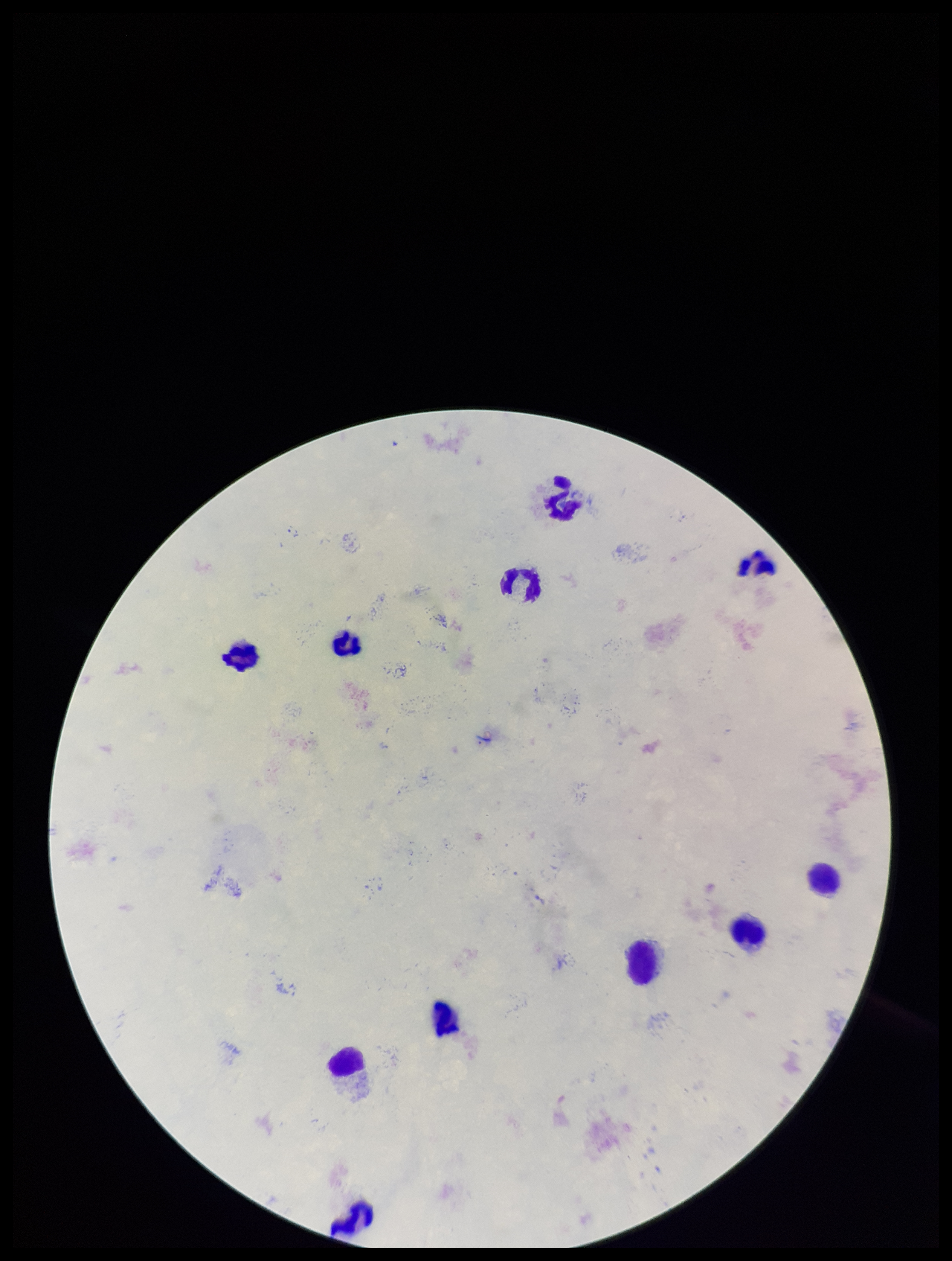

Leukocyte count: 11. Plasmodium parasites: none identified. Preparation: thick smear. Smartphone photograph taken through the eyepiece of a microscope. Image is 952×1261 pixels. Stained with Giemsa. Parasite count: 0. Patient malaria status: negative. One field from this slide.